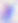

magnification: 400x
identification: Toxoplasma gondii
modality: micrograph